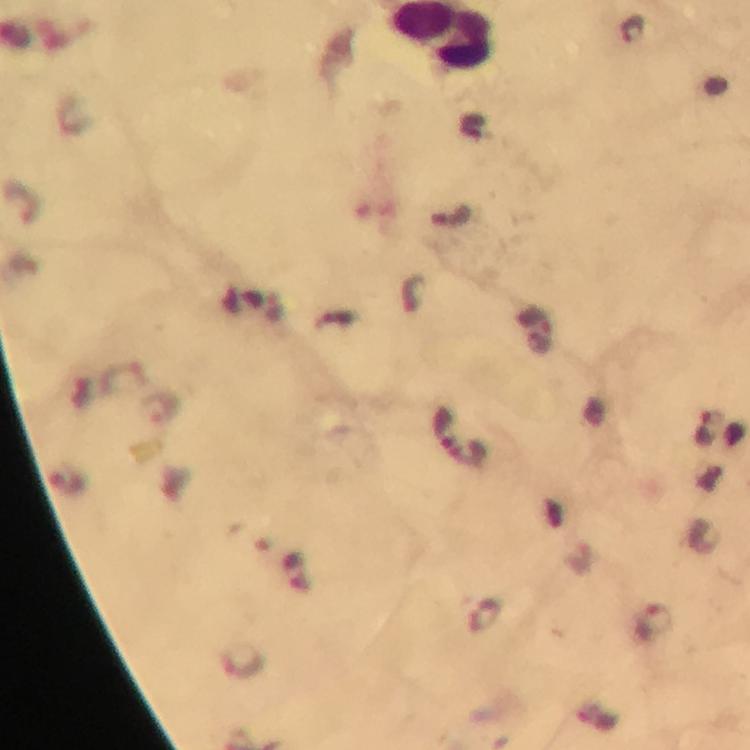
image_size: 750×750 pixels
preparation: thick blood film
capture: smartphone photograph through a microscope
plasmodium_parasite_locations: 'approximate centers as [x, y] in pixels: [633, 29], [451, 218], [535, 333], [161, 409], [707, 431], [459, 440], [67, 483], [298, 571], [656, 621]'
stain: Giemsa
context: from a diagnostic examination for malaria
immersion_oil: applied
cropped_from: one field of view
magnification: 100x